Locate every Plasmodium vivax-infected red blood cell.
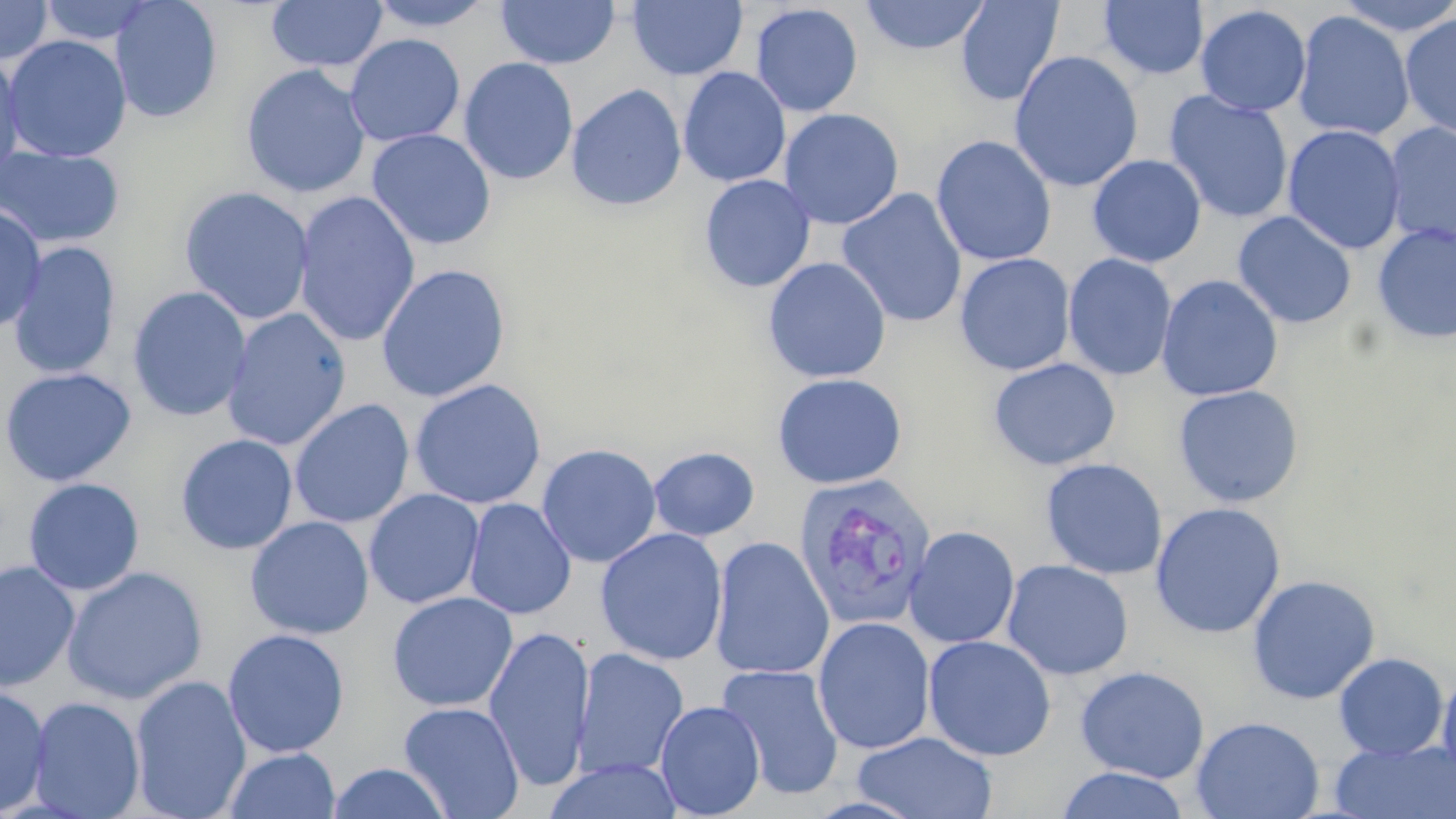
Approximate bounding boxes as [x1, y1, x2, y2] in pixels.
Plasmodium vivax-infected red blood cells: [792, 472, 938, 631].

Summary:
  - Uninfected red blood cell locations: [109, 0, 223, 123], [266, 0, 387, 72], [496, 0, 620, 69], [859, 0, 991, 55], [955, 0, 1063, 106], [1333, 0, 1456, 37], [0, 1, 54, 65], [37, 1, 160, 46], [366, 1, 497, 32], [628, 1, 747, 81], [1097, 1, 1209, 80], [750, 3, 863, 117], [1195, 4, 1312, 116], [1293, 11, 1415, 141], [1399, 13, 1456, 140], [2, 34, 132, 163], [344, 34, 465, 147], [0, 50, 26, 186], [1008, 50, 1144, 193], [458, 57, 579, 185], [240, 65, 371, 198], [678, 67, 791, 188], [566, 84, 687, 211], [1164, 90, 1294, 224], [778, 107, 904, 229], [1383, 122, 1456, 248], [1282, 124, 1405, 255], [366, 128, 496, 250], [931, 134, 1056, 267], [0, 146, 125, 250], [1087, 154, 1206, 267], [699, 174, 816, 292], [178, 186, 315, 325], [836, 188, 968, 328], [293, 190, 420, 348], [0, 204, 47, 335], [1231, 211, 1357, 329], [1372, 223, 1456, 344], [7, 242, 121, 380], [955, 253, 1076, 376], [1062, 253, 1177, 381], [763, 256, 891, 383], [376, 263, 511, 402], [1156, 274, 1284, 401], [128, 286, 251, 422], [221, 307, 352, 451], [988, 357, 1121, 471], [0, 367, 137, 487], [771, 372, 908, 489], [409, 378, 547, 510], [1172, 385, 1304, 508], [289, 399, 414, 529], [175, 433, 298, 555], [537, 443, 661, 568], [647, 446, 760, 542], [1040, 458, 1168, 580], [23, 478, 145, 595], [364, 488, 484, 609], [463, 498, 577, 619], [1149, 502, 1287, 639], [245, 516, 374, 639], [903, 525, 1020, 649], [595, 527, 729, 665], [709, 536, 834, 680], [0, 559, 81, 692], [1001, 559, 1134, 681], [62, 567, 207, 704], [1246, 574, 1381, 705], [387, 591, 518, 712], [813, 617, 935, 755], [483, 625, 595, 793], [223, 628, 350, 758], [923, 635, 1056, 761], [573, 649, 689, 780], [1333, 652, 1449, 759], [716, 664, 845, 800], [1075, 665, 1210, 784], [1436, 666, 1456, 792], [129, 675, 252, 819], [0, 685, 51, 817], [27, 696, 146, 818], [655, 700, 765, 818], [398, 701, 525, 819], [1191, 716, 1324, 819], [852, 731, 999, 819], [1329, 738, 1456, 819], [223, 748, 341, 819], [544, 759, 683, 819], [326, 763, 453, 819], [1054, 766, 1190, 819]
  - Slide-level diagnosis: Plasmodium vivax
  - Stain: May-Grünwald-Giemsa
  - Magnification: 1000x
  - Image size: 1456×819 pixels
  - Preparation: thin blood film
  - Field of view: one of a larger specimen
  - Modality: light microscopy